Describe the morphology of the red blood cells.
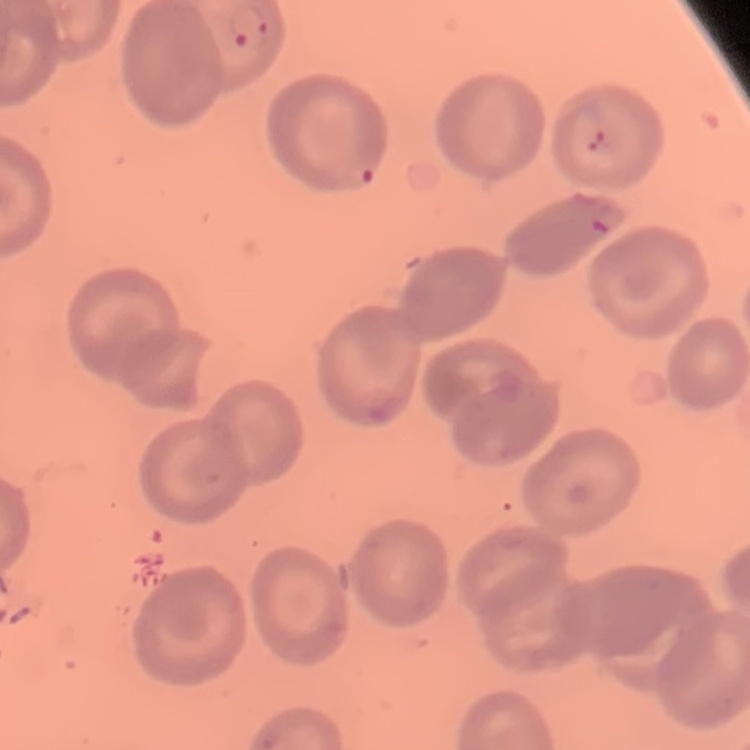
They show no rouleaux formation.

{
  "image_type": "square crop of a larger photomicrograph",
  "preparation": "thin blood film",
  "stain": "Field's or Giemsa"
}